Locate every leukocyte (white blood cell).
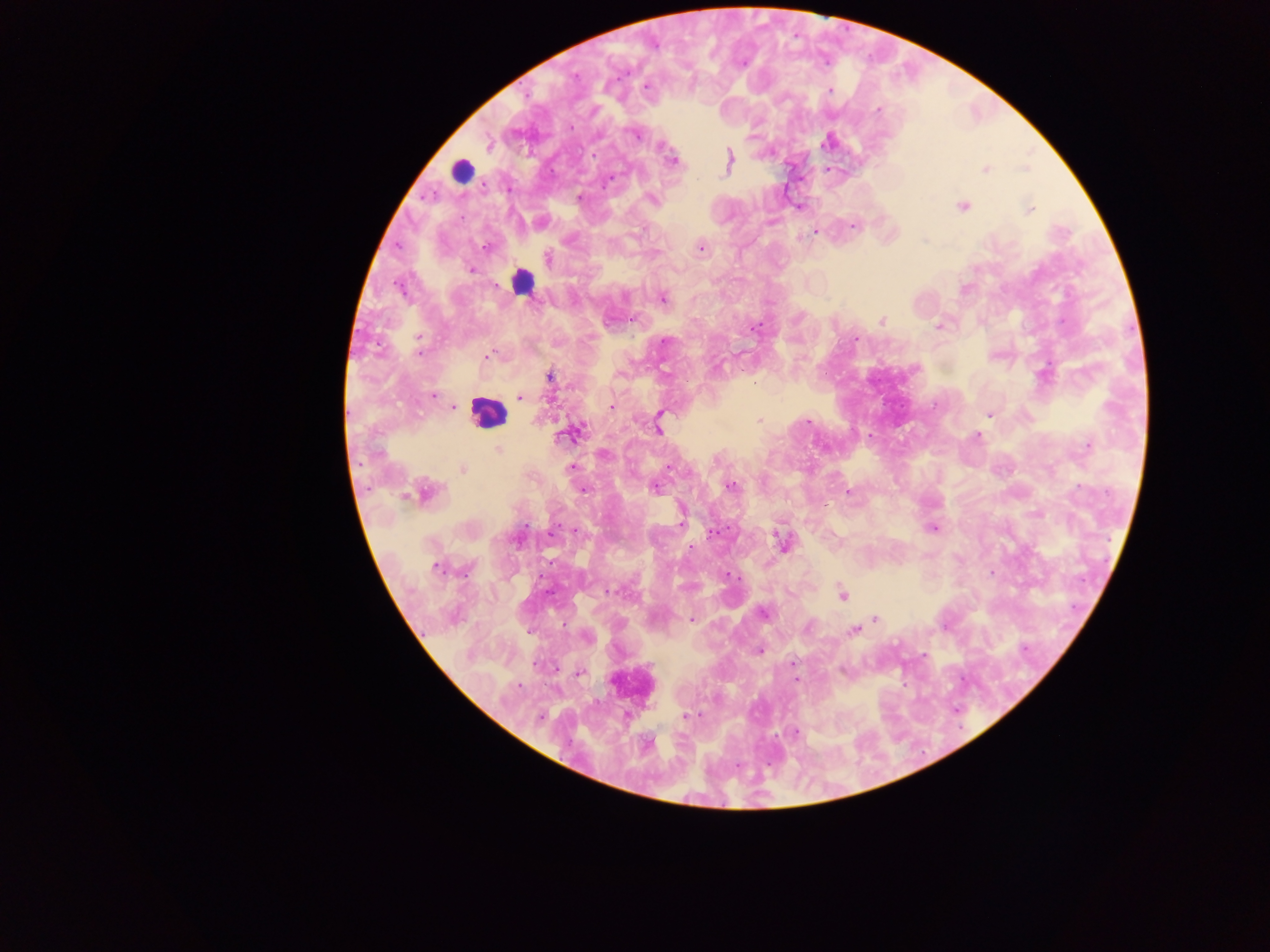

Approximate centers as x y in pixels.
Leukocytes: 461 171; 522 281; 487 414; 632 684.

Summary:
  - Plasmodium parasite locations: 646 87; 830 90; 878 110; 570 128; 635 135; 488 143; 672 161; 729 161; 986 168; 579 198; 653 200; 963 207; 1030 209; 853 226; 814 232; 396 247; 484 247; 700 248; 548 259; 472 270; 400 289; 624 296; 663 299; 881 320; 938 325; 756 328; 419 337; 855 340; 665 342; 419 353; 487 355; 550 377; 433 395; 520 397; 611 405; 453 406; 988 414; 660 415; 759 420; 808 421; 658 428; 568 434; 870 436; 977 436; 1087 446; 498 450; 603 454; 669 466; 572 467; 464 469; 731 486; 655 488; 583 491; 426 492; 848 492; 681 520; 526 523; 933 528; 574 531; 713 532; 782 542; 691 547; 436 567; 992 573; 727 574; 550 591; 611 591; 843 594; 1076 606; 763 612; 876 618; 691 620; 854 631; 528 632; 587 637; 1023 646; 760 650; 924 656; 793 663; 579 672; 963 678; 905 685; 955 707; 686 715; 540 717; 795 732
  - Country: Ghana
  - Preparation: thick blood film
  - Field of view: single
  - Image size: 1270×952 pixels
  - Capture: mobile-phone photograph through a microscope